Assess the morphology of the red blood cells.
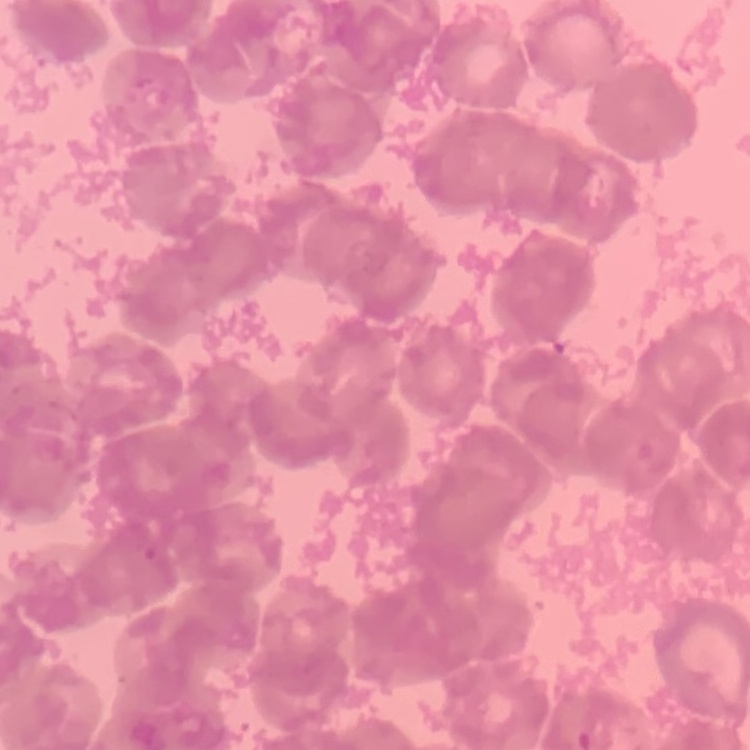
Rouleaux formation.

Stained with either Field's or Giemsa. Thin blood film. Square crop of a larger photomicrograph.